Point out each malaria parasite.
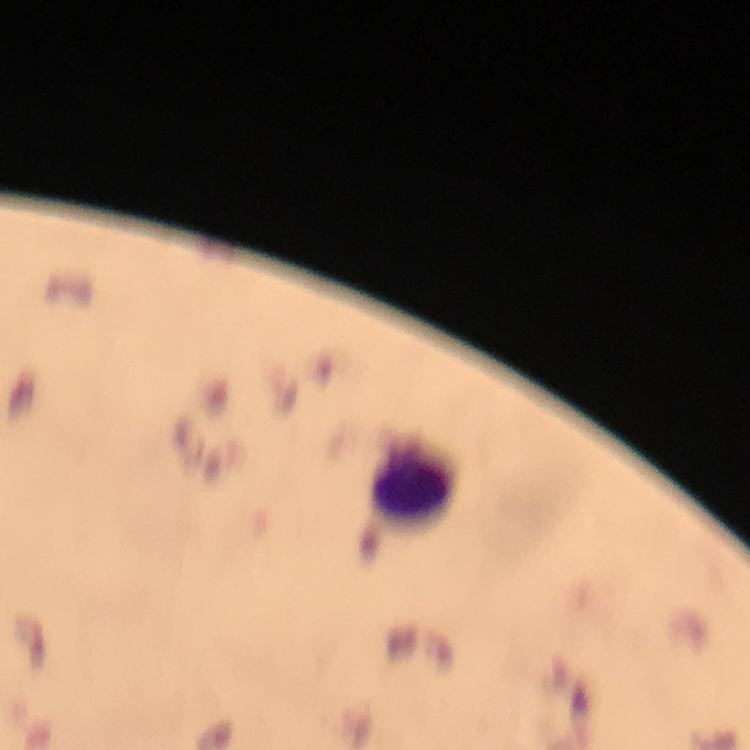
No malaria parasites detected.

Approximate centers as [x, y] in pixels. Leukocyte locations: [413, 482]. Image is 750×750 pixels. A crop from one field of view. Smartphone photograph taken through a microscope. Immersion oil applied. Giemsa-stained preparation. At 100x magnification. Thick blood film. From a malaria diagnostic workup.